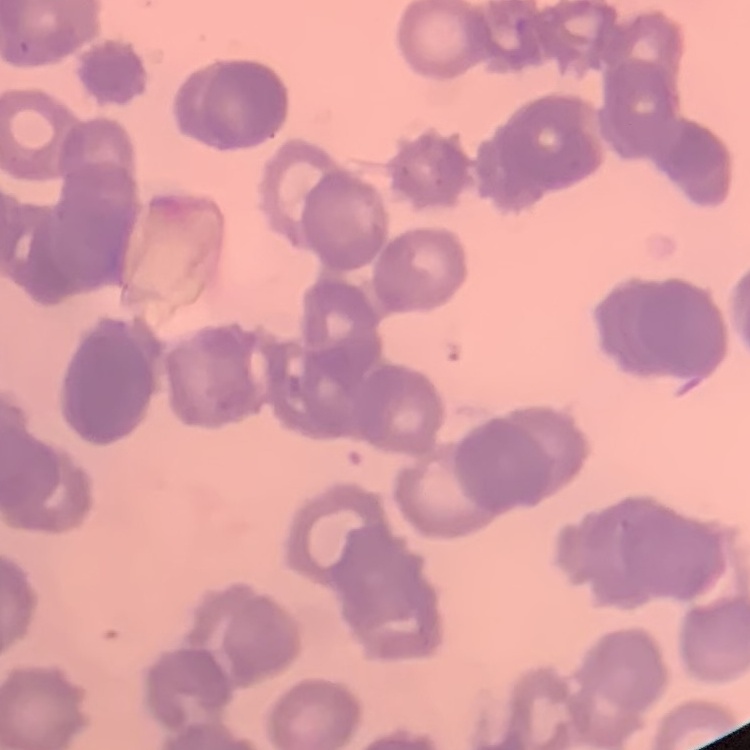

Summary:
  - Red blood cell morphology: rouleaux formation
  - Image type: one tile cut from a larger photomicrograph
  - Stain: Field's or Giemsa
  - Preparation: thin blood film